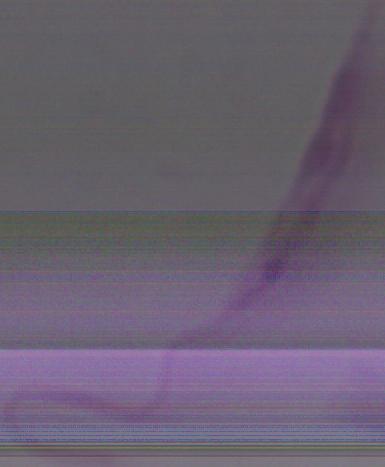

1000x magnification. Micrograph. A Leishmania parasite is shown.